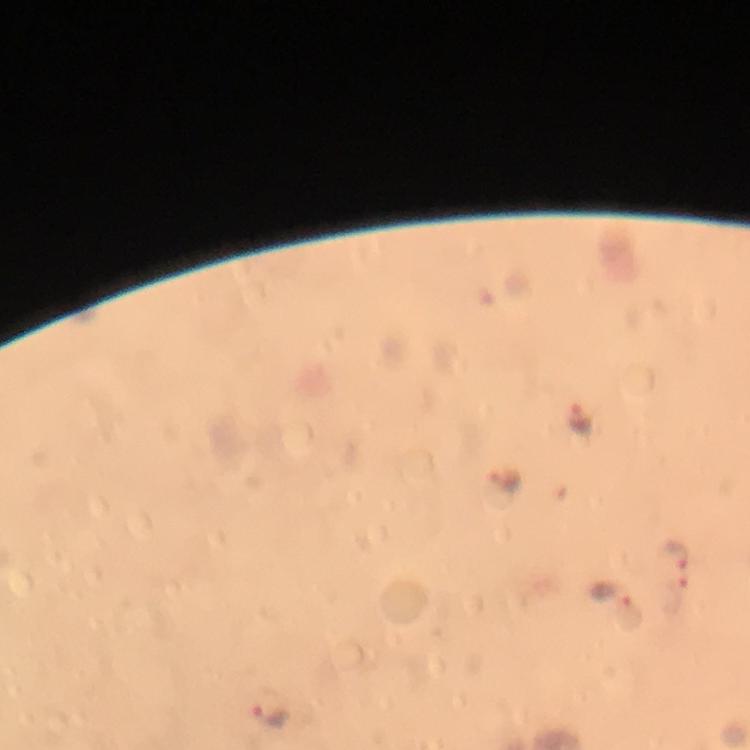
context = from a diagnostic examination for malaria
preparation = thick smear
image size = 750×750 pixels
magnification = 100x
capture = smartphone mounted on the microscope
Plasmodium parasite locations = approximate centers as [x, y] in pixels: [582, 418], [502, 481], [677, 553], [611, 593], [268, 713]
cropped from = a single field of view
stain = Giemsa
immersion oil = applied